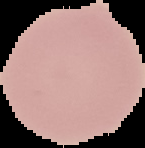

Image is 145×148 pixels. Segmented cell region on a black background. Malaria status: uninfected. From a thin blood smear.